Assess this cell for malaria.
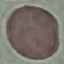

Uninfected.

{
  "capture": "smartphone camera at the microscope eyepiece",
  "stain": "Giemsa",
  "image_type": "automatically extracted cell patch, resized to 64 × 64 pixels",
  "preparation": "thin blood film"
}